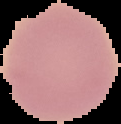
Image is 121×124 pixels. From a thin blood film. The area outside the segmented cell region is set to black. Result: no malaria parasites seen.